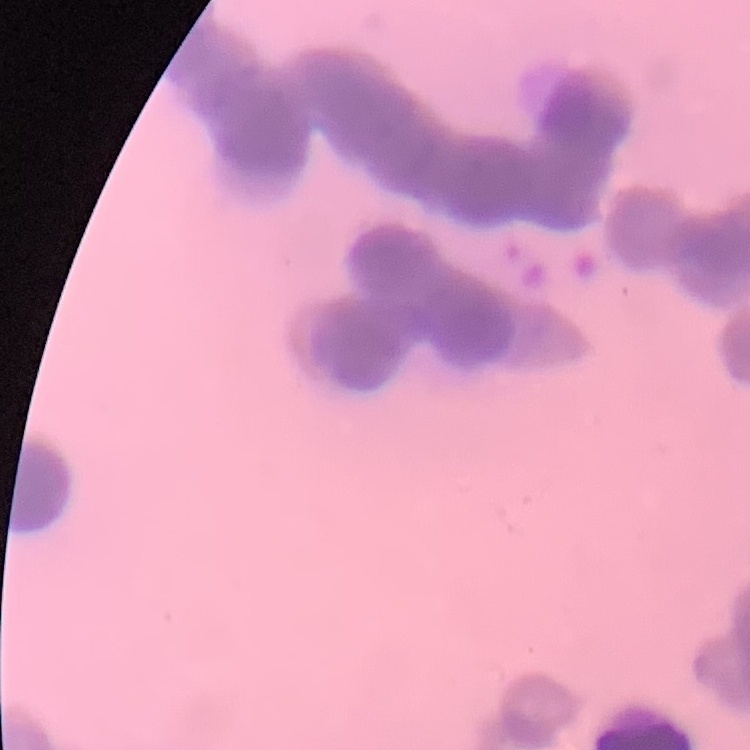
erythrocyte morphology = rouleaux formation
stain = Field's or Giemsa
image type = one tile cut from a larger photomicrograph
preparation = thin peripheral smear